Locate and identify every blood parasite.
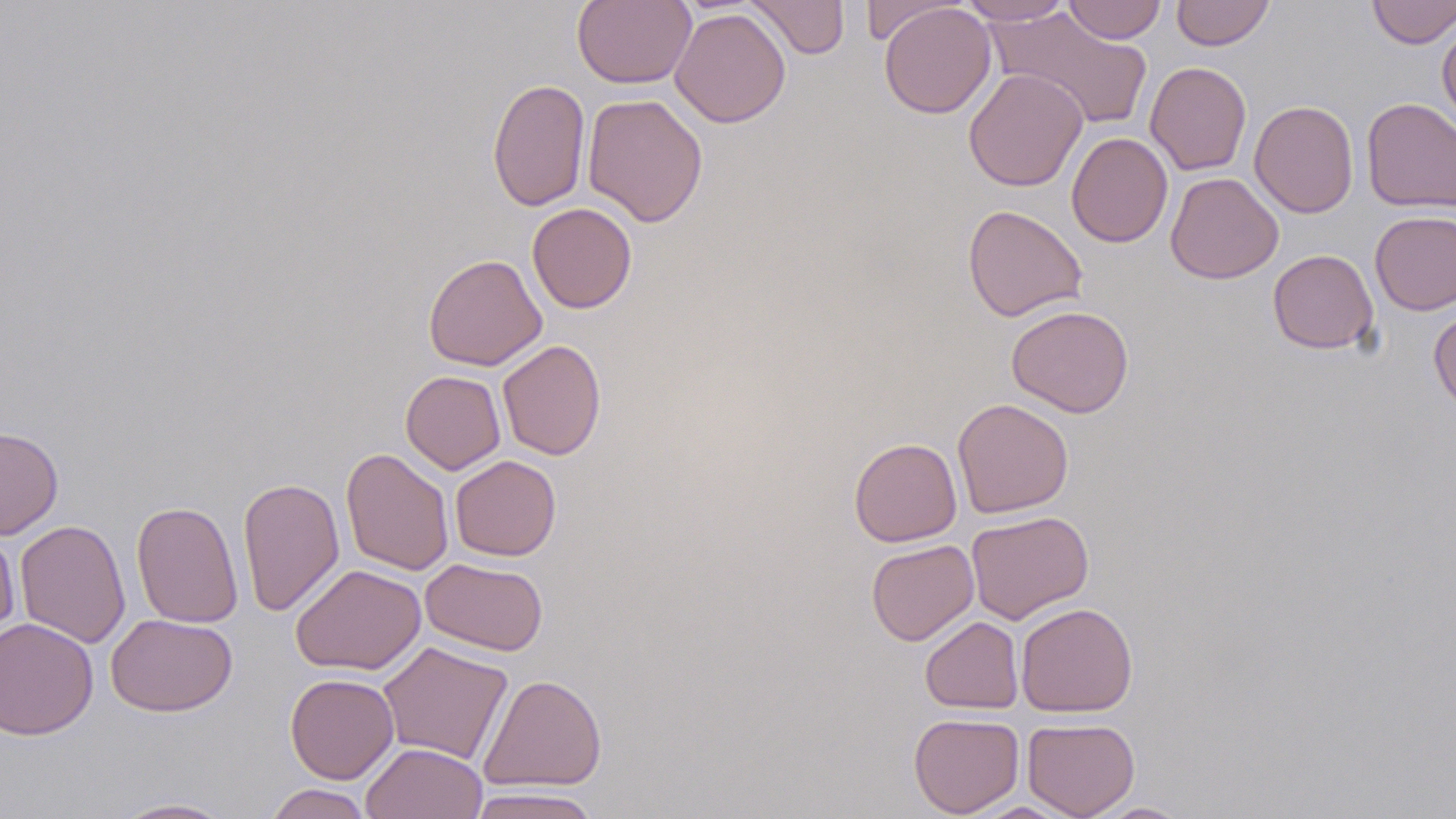
No blood parasites seen.

Approximate bounding boxes as (x1, y1, x2, y2) in pixels. Uninfected red blood cell locations: (572, 0, 696, 89), (744, 0, 850, 60), (859, 0, 963, 45), (958, 0, 1074, 25), (1063, 0, 1166, 44), (1171, 0, 1274, 51), (1366, 0, 1456, 49), (878, 3, 996, 119), (989, 7, 1153, 130), (670, 8, 791, 127), (1437, 19, 1456, 136), (1145, 61, 1252, 176), (963, 68, 1088, 191), (487, 78, 590, 211), (582, 93, 708, 227), (1361, 98, 1456, 213), (1249, 100, 1358, 218), (1066, 132, 1173, 248), (1165, 172, 1284, 284), (527, 202, 637, 313), (962, 204, 1088, 322), (1370, 210, 1456, 315), (1267, 249, 1379, 354), (423, 253, 547, 371), (1429, 304, 1456, 417), (1006, 305, 1134, 418), (498, 340, 606, 460), (400, 370, 506, 475), (952, 397, 1074, 518), (0, 426, 64, 540), (849, 437, 962, 547), (340, 447, 454, 576), (449, 455, 561, 561), (237, 477, 344, 617), (131, 500, 243, 629), (966, 510, 1094, 624), (14, 519, 131, 648), (0, 526, 20, 643), (866, 540, 979, 645), (420, 558, 549, 656), (290, 564, 427, 675), (1015, 602, 1138, 718), (106, 613, 238, 716), (0, 616, 99, 741), (920, 616, 1024, 714), (377, 641, 513, 766), (285, 673, 399, 783), (478, 673, 607, 793), (908, 713, 1025, 817), (1023, 718, 1140, 819), (361, 742, 487, 819), (263, 783, 374, 819), (467, 787, 601, 819), (109, 798, 238, 818), (964, 801, 1080, 818), (1090, 801, 1192, 818). Slide-level diagnosis: negative for blood parasites. Light microscopy. Captured at 1000x magnification. May-Grünwald-Giemsa-stained preparation. Image is 1456×819 pixels. One field of a larger specimen. Thin blood film.